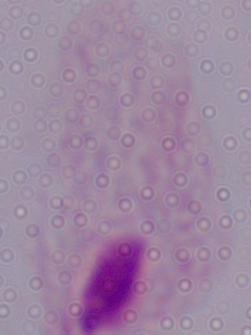
Summary:
  - Modality: micrograph
  - Magnification: 1000x
  - Identification: trichomonad